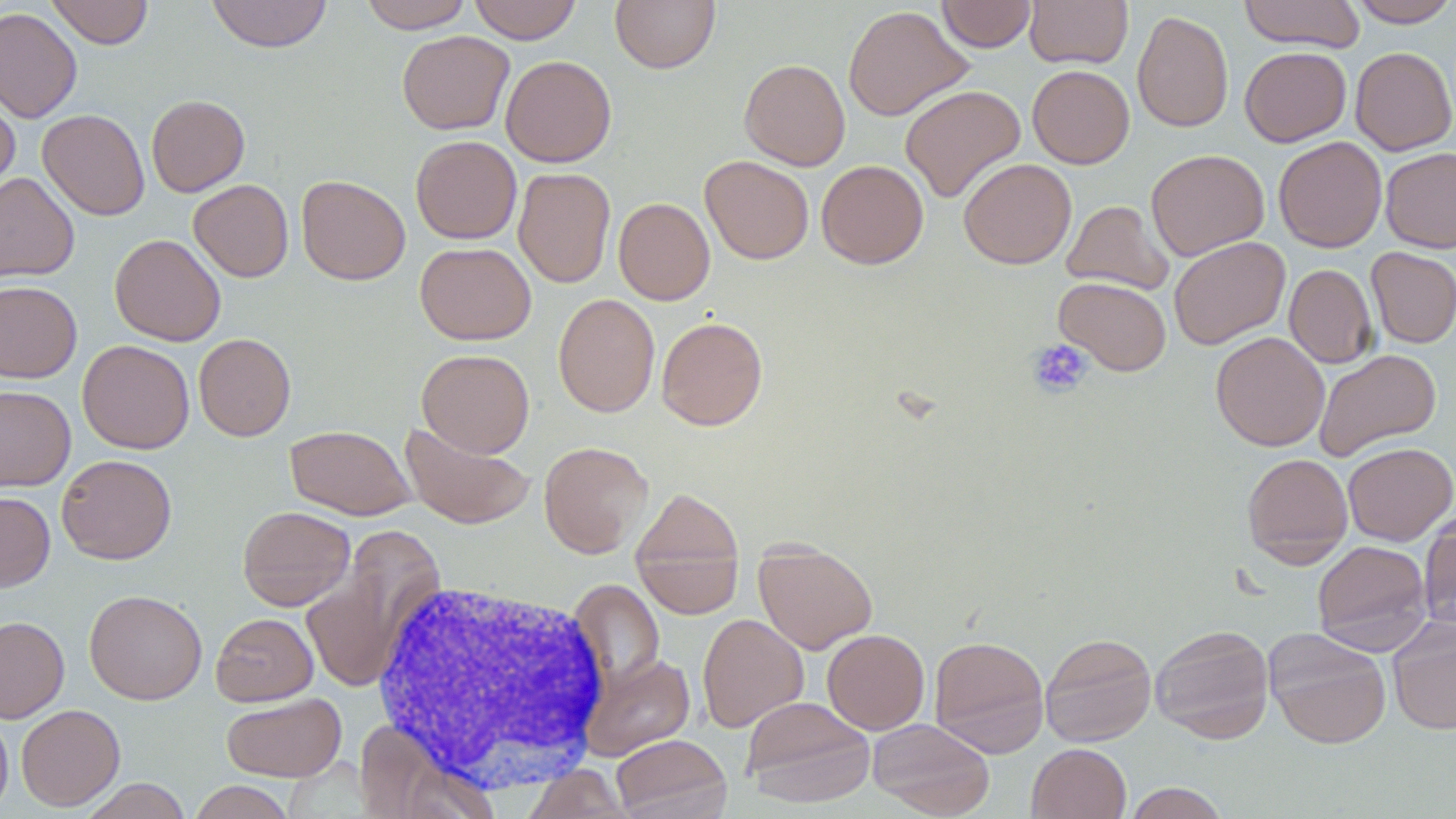
Approximate bounding boxes as (x1, y1, x2, y2) in pixels. Uninfected red blood cell locations: (46, 0, 154, 49), (206, 0, 332, 53), (359, 0, 474, 33), (468, 0, 582, 44), (610, 0, 720, 73), (937, 0, 1036, 52), (1025, 0, 1133, 69), (1238, 0, 1366, 52), (1347, 0, 1456, 27), (843, 5, 973, 121), (0, 7, 82, 123), (1132, 10, 1233, 133), (396, 30, 514, 135), (1239, 46, 1351, 147), (1350, 46, 1456, 155), (500, 55, 616, 167), (740, 59, 850, 171), (1027, 64, 1134, 168), (900, 84, 1026, 203), (0, 88, 20, 196), (146, 94, 249, 197), (38, 109, 150, 220), (410, 135, 522, 244), (1273, 136, 1387, 253), (1380, 147, 1456, 253), (1145, 148, 1269, 261), (700, 156, 814, 264), (958, 158, 1077, 269), (816, 160, 929, 269), (513, 168, 615, 288), (0, 172, 80, 284), (297, 175, 410, 285), (189, 179, 294, 282), (614, 197, 715, 305), (1062, 200, 1174, 295), (109, 233, 226, 346), (1168, 236, 1290, 350), (415, 242, 536, 345), (1366, 247, 1456, 348), (1284, 264, 1378, 368), (1054, 277, 1172, 376), (0, 279, 82, 383), (553, 293, 660, 418), (656, 316, 768, 431), (1210, 331, 1330, 452), (194, 333, 296, 441), (78, 340, 194, 454), (1314, 348, 1442, 461), (416, 349, 535, 457), (0, 385, 75, 492), (400, 421, 535, 531), (284, 425, 415, 519), (538, 441, 654, 558), (1342, 442, 1456, 545), (1242, 453, 1353, 565), (56, 454, 177, 564), (630, 487, 745, 615), (0, 492, 55, 591), (237, 506, 355, 610), (1419, 513, 1456, 630), (1312, 539, 1432, 655), (753, 542, 878, 655), (299, 552, 425, 693), (568, 580, 665, 688), (84, 589, 207, 704), (211, 613, 318, 706), (697, 613, 809, 733), (0, 616, 70, 723), (1387, 617, 1456, 735), (1150, 624, 1275, 743), (1264, 628, 1391, 749), (822, 629, 930, 734), (1040, 632, 1157, 747), (929, 635, 1049, 757), (581, 653, 695, 760), (221, 694, 346, 782), (741, 696, 875, 807), (16, 704, 125, 811), (0, 710, 13, 817), (868, 718, 995, 818), (354, 719, 501, 818), (611, 734, 731, 819), (1026, 743, 1131, 819), (520, 763, 634, 819), (80, 778, 192, 818), (188, 781, 297, 819), (1124, 782, 1230, 818). Platelet locations: (1027, 339, 1093, 398). White blood cell locations: (370, 578, 611, 794). Slide-level diagnosis: negative for blood parasites. Image is 1456×819 pixels. May-Grünwald-Giemsa-stained preparation. One field of a larger specimen. 1000x magnification. Light microscopy. Thin blood smear.